Name the parasite shown.
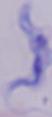

A trypanosome.

1000x magnification. Photomicrograph.